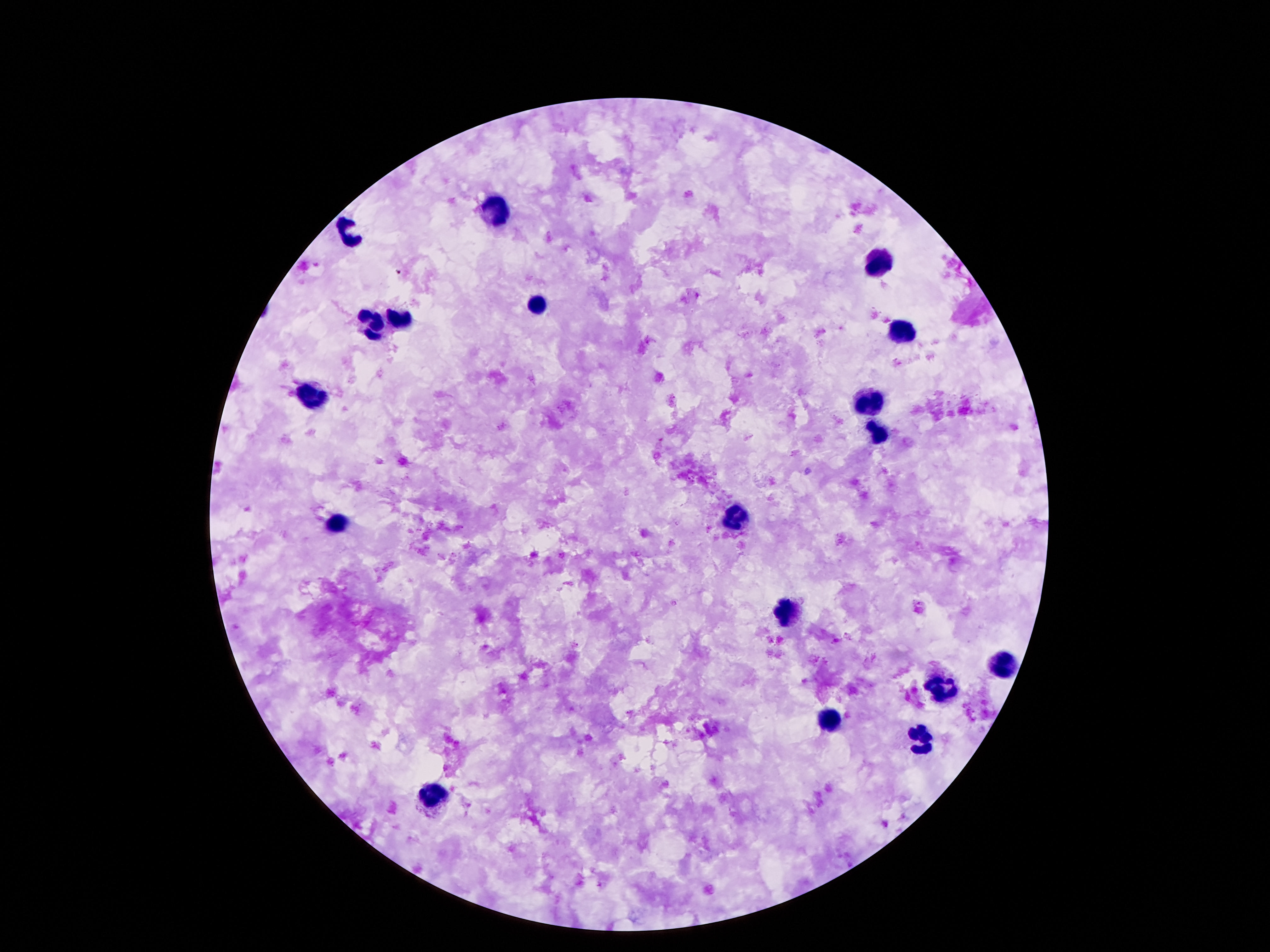

Approximate centers as [x, y] in pixels.
Summary:
  - Leukocyte locations: [492, 208], [353, 235], [876, 262], [536, 306], [397, 318], [376, 323], [903, 328], [315, 397], [870, 399], [878, 436], [739, 516], [340, 526], [786, 614], [1002, 666], [943, 688], [832, 718], [920, 740], [433, 795]
  - Stain: Giemsa
  - Field of view: one from this slide
  - Capture: smartphone camera through the microscope eyepiece
  - Magnification: 100x
  - Image size: 1270×952 pixels
  - Patient malaria status: uninfected
  - Preparation: thick blood smear